Report the malaria status of this cell.
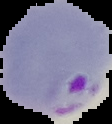

It is parasitized.

Summary:
  - Image type: segmented cell region on a black background
  - Preparation: thin blood film
  - Image size: 112×124 pixels